State the preparation type.
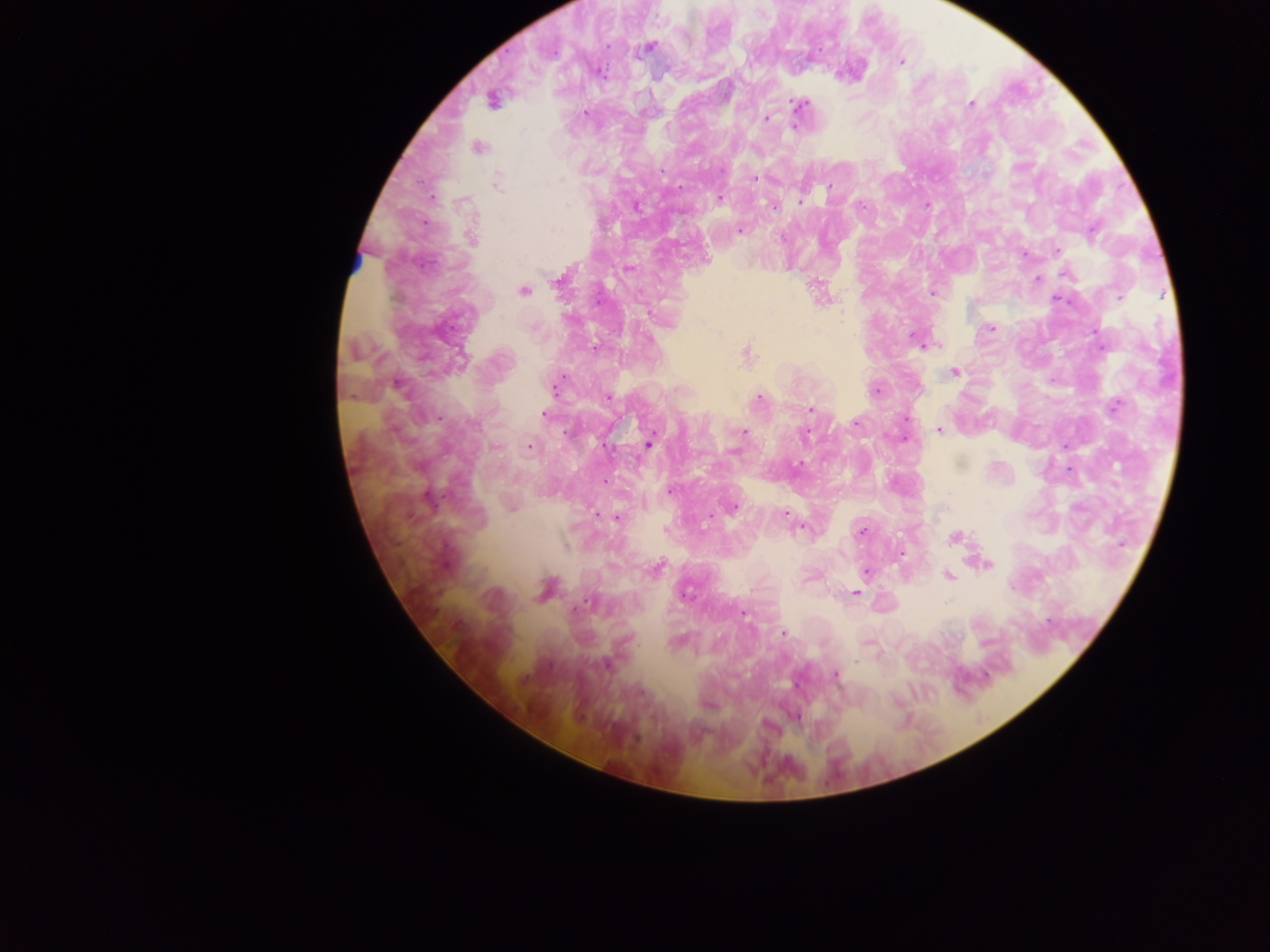
This is a thick smear.

field of view = single
country = Ghana
malaria parasite locations = approximate centers as [x, y] in pixels: [647, 47], [901, 61], [492, 100], [971, 104], [800, 105], [586, 113], [766, 118], [478, 147], [755, 179], [497, 182], [830, 189], [718, 199], [801, 199], [774, 206], [862, 206], [740, 230], [1093, 232], [472, 239], [1057, 250], [628, 268], [1065, 274], [1037, 279], [559, 280], [523, 291], [933, 293], [1119, 297], [1059, 300], [989, 329], [914, 337], [745, 354], [954, 372], [397, 385], [555, 386], [875, 391], [608, 397], [759, 398], [1115, 406], [811, 409], [545, 414], [856, 423], [939, 430], [744, 432], [806, 434], [649, 443], [530, 447], [734, 452], [670, 491], [733, 508], [617, 516], [786, 516], [862, 531], [956, 538], [988, 563], [657, 568], [866, 572], [948, 575], [1012, 588], [546, 589], [855, 593], [686, 594], [581, 605], [745, 614], [784, 633], [605, 665], [836, 675], [708, 706], [795, 716]
capture = mobile-phone photograph through a microscope
image size = 1270×952 pixels